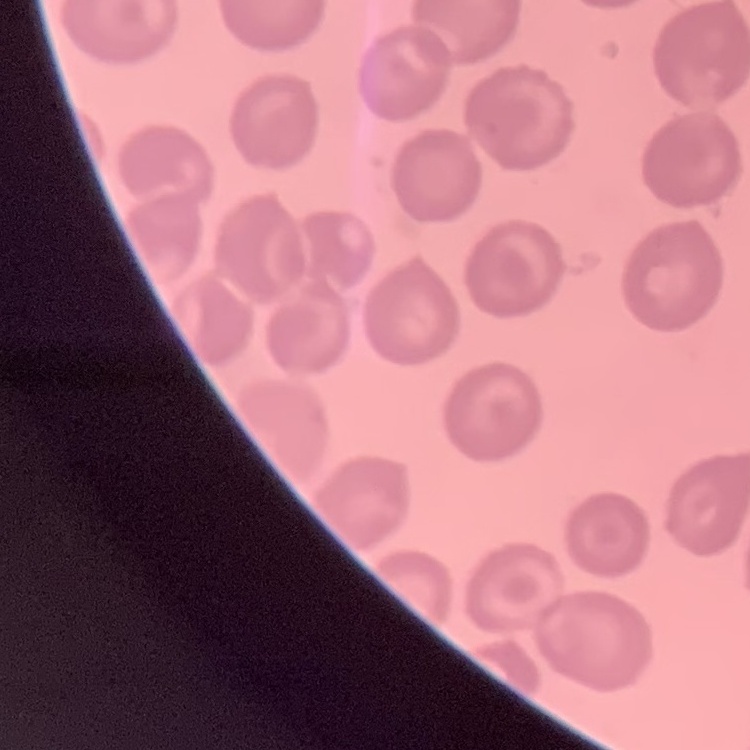 The red blood cells show no rouleaux formation. Field's or Giemsa stain. Square crop of a larger photomicrograph. Thin peripheral smear.